State the blood parasite species.
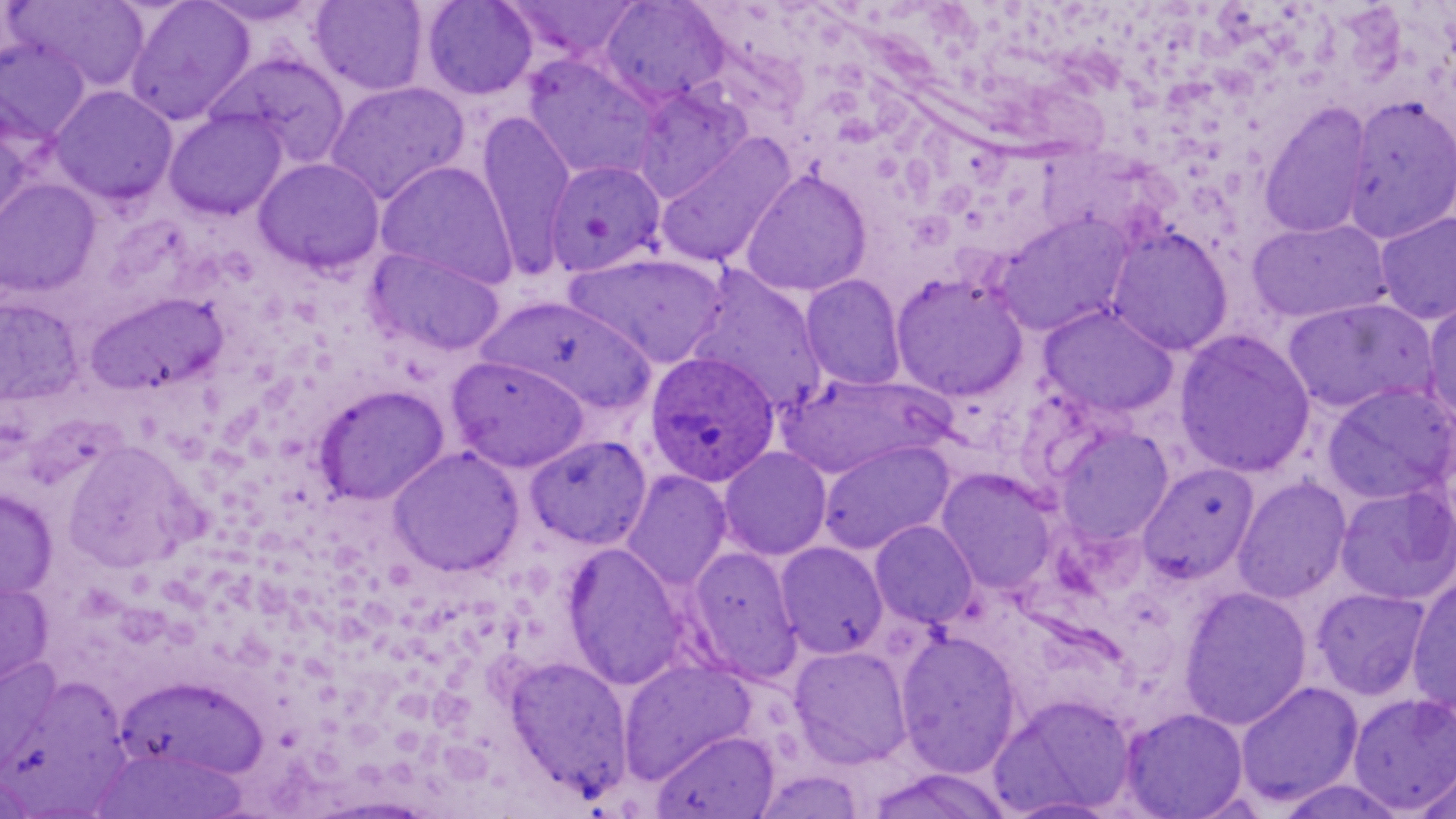
Plasmodium ovale.

Approximate bounding boxes as (x1, y1, x2, y2) in pixels. Plasmodium ovale-infected red blood cell locations: (645, 351, 781, 488). Uninfected red blood cell locations: (6, 0, 152, 92), (124, 0, 255, 125), (197, 0, 323, 27), (421, 0, 538, 100), (503, 0, 646, 62), (309, 1, 429, 95), (598, 1, 731, 107), (0, 38, 92, 149), (208, 53, 351, 168), (523, 54, 662, 182), (324, 80, 469, 204), (50, 85, 177, 205), (632, 85, 752, 202), (1341, 94, 1456, 245), (1259, 102, 1374, 240), (164, 109, 287, 221), (476, 111, 576, 276), (0, 119, 35, 236), (654, 132, 796, 269), (253, 157, 386, 276), (543, 159, 667, 277), (376, 160, 518, 290), (739, 169, 871, 297), (0, 178, 101, 298), (1375, 211, 1456, 324), (993, 213, 1134, 337), (1247, 219, 1392, 325), (1106, 227, 1233, 356), (366, 246, 506, 356), (563, 252, 729, 367), (691, 272, 829, 415), (890, 272, 1028, 401), (800, 275, 907, 391), (87, 291, 226, 397), (0, 296, 82, 408), (481, 296, 657, 415), (1421, 296, 1456, 426), (1283, 298, 1437, 414), (1038, 305, 1178, 418), (1174, 329, 1315, 479), (448, 356, 591, 472), (776, 373, 951, 479), (1322, 383, 1456, 505), (314, 385, 449, 505), (1054, 425, 1174, 546), (526, 435, 651, 549), (62, 439, 199, 573), (818, 440, 953, 554), (388, 445, 524, 577), (719, 447, 832, 560), (1138, 463, 1259, 584), (936, 468, 1057, 594), (622, 471, 732, 590), (1233, 477, 1351, 604), (1335, 483, 1455, 605), (0, 488, 58, 602), (870, 520, 978, 629), (775, 541, 888, 658), (563, 543, 688, 690), (687, 547, 803, 682), (1407, 574, 1456, 717), (0, 576, 54, 694), (1178, 586, 1312, 730), (1312, 588, 1430, 700), (895, 629, 1022, 778), (789, 645, 913, 768), (0, 655, 64, 775), (504, 656, 632, 798), (619, 659, 755, 782), (0, 666, 120, 801), (114, 675, 267, 781), (1235, 681, 1363, 807), (989, 692, 1138, 816), (1349, 693, 1456, 813), (1118, 707, 1249, 819), (651, 729, 779, 819), (90, 747, 250, 818), (1413, 759, 1456, 819), (1, 768, 38, 817), (1274, 777, 1408, 819). Thin blood film. May-Grünwald-Giemsa stain. Image is 1456×819 pixels. Light microscopy. 1000x magnification. One field of a larger specimen.